Classify this cell by malaria status.
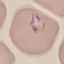

It is parasitized.

preparation: thin blood smear
stain: Giemsa
capture: smartphone camera at the microscope eyepiece
image_type: automatically extracted cell patch, resized to 64 × 64 pixels